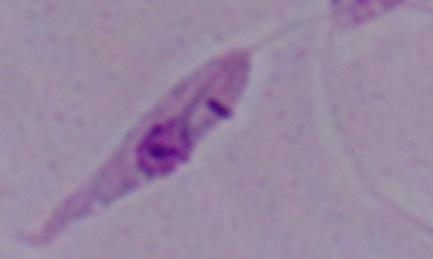
{
  "identification": "Leishmania",
  "modality": "photomicrograph",
  "magnification": "1000x"
}